Locate every Plasmodium vivax-infected red blood cell.
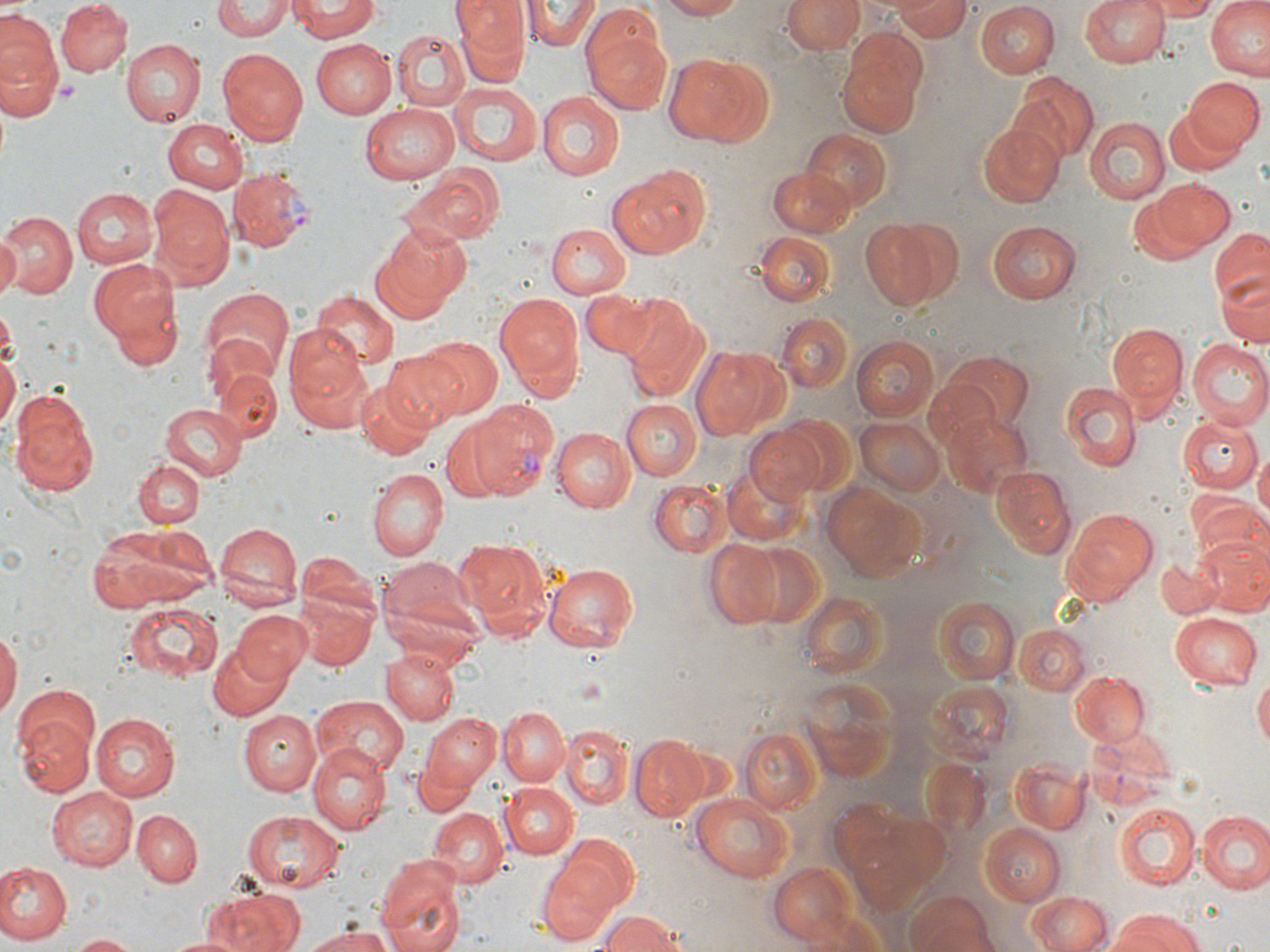

Approximate bounding boxes as (x1, y1, x2, y2) in pixels.
Plasmodium vivax-infected red blood cells: (230, 169, 316, 252), (469, 400, 558, 497).

slide_level_diagnosis: Plasmodium vivax
preparation: thin blood smear
uninfected_red_blood_cell_locations: 'approximate bounding boxes as (x1, y1, x2, y2) in pixels: (57, 0, 131, 75), (213, 0, 291, 41), (454, 0, 526, 81), (662, 0, 749, 21), (781, 0, 863, 54), (1081, 0, 1169, 68), (1151, 0, 1220, 19), (1206, 0, 1269, 81), (289, 1, 379, 42), (526, 1, 598, 54), (890, 1, 972, 40), (976, 1, 1060, 78), (581, 5, 672, 113), (0, 12, 63, 99), (393, 30, 470, 111), (311, 39, 396, 117), (836, 39, 929, 138), (121, 40, 205, 127), (218, 47, 308, 144), (0, 49, 61, 122), (663, 50, 776, 146), (1010, 75, 1097, 162), (1183, 77, 1261, 155), (452, 84, 543, 166), (537, 92, 624, 180), (359, 105, 458, 184), (1165, 109, 1240, 176), (1085, 117, 1170, 204), (162, 119, 248, 194), (979, 122, 1064, 207), (803, 130, 893, 215), (604, 164, 712, 260), (767, 167, 860, 236), (402, 175, 497, 245), (1153, 179, 1236, 250), (150, 183, 235, 290), (72, 187, 157, 270), (1127, 192, 1215, 266), (2, 211, 78, 298), (861, 216, 958, 311), (988, 220, 1081, 303), (544, 223, 630, 299), (369, 227, 466, 322), (1209, 228, 1270, 305), (754, 231, 834, 305), (0, 235, 20, 297), (89, 257, 182, 356), (1214, 271, 1269, 348), (200, 286, 293, 381), (581, 292, 664, 359), (311, 293, 398, 369), (495, 294, 583, 391), (621, 301, 708, 400), (776, 314, 854, 395), (1107, 324, 1189, 410), (284, 325, 369, 424), (419, 335, 503, 418), (850, 336, 940, 422), (1186, 340, 1270, 430), (0, 346, 18, 437), (691, 346, 787, 441), (382, 350, 467, 431), (935, 351, 1036, 432), (213, 366, 282, 445), (922, 378, 1000, 456), (357, 379, 437, 458), (1061, 382, 1142, 471), (11, 387, 99, 493), (619, 399, 701, 479), (159, 404, 247, 482), (940, 411, 1033, 500), (773, 413, 853, 495), (1179, 416, 1262, 493), (854, 417, 945, 495), (440, 423, 513, 502), (743, 424, 832, 508), (551, 428, 636, 514), (1254, 450, 1270, 524), (134, 460, 203, 529), (991, 466, 1075, 559), (368, 467, 448, 560), (649, 480, 730, 557), (823, 482, 928, 579), (1188, 497, 1269, 573), (1062, 508, 1158, 602), (214, 523, 301, 610), (88, 525, 217, 612), (454, 536, 552, 641), (1195, 536, 1270, 616), (704, 539, 791, 629), (745, 541, 827, 631), (299, 553, 377, 618), (1156, 555, 1220, 620), (382, 556, 483, 642), (544, 563, 638, 650), (799, 588, 886, 679), (296, 592, 378, 672), (931, 598, 1021, 686), (122, 600, 225, 683), (231, 610, 315, 683), (1169, 612, 1262, 690), (1013, 624, 1090, 696), (0, 631, 19, 723), (207, 641, 293, 719), (383, 649, 461, 725), (1069, 669, 1151, 747), (1254, 672, 1270, 750), (795, 675, 901, 782), (10, 687, 100, 796), (311, 696, 409, 780), (501, 707, 570, 785), (238, 711, 320, 796), (420, 712, 502, 793), (90, 714, 178, 800), (559, 725, 632, 809), (739, 727, 823, 816), (1087, 727, 1177, 778), (630, 738, 707, 819), (308, 744, 394, 833), (1010, 765, 1094, 835), (500, 781, 578, 858), (46, 784, 140, 868), (689, 795, 794, 882), (1117, 804, 1199, 890), (426, 807, 508, 890), (241, 809, 344, 894), (133, 810, 201, 885), (1197, 811, 1270, 895), (979, 822, 1067, 906), (557, 831, 639, 910), (376, 853, 467, 950), (537, 857, 622, 944), (0, 863, 71, 944), (767, 863, 859, 945), (204, 889, 307, 952), (906, 892, 998, 952), (1028, 892, 1114, 952), (597, 911, 685, 952), (1106, 911, 1202, 952), (304, 927, 399, 952), (71, 933, 140, 952), (166, 934, 242, 952)'
field_of_view: one of a larger specimen
modality: optical microscopy
image_size: 1270×952 pixels
magnification: 1000x
platelet_locations: 'approximate bounding boxes as (x1, y1, x2, y2) in pixels: (54, 78, 79, 107)'
stain: May-Grünwald-Giemsa